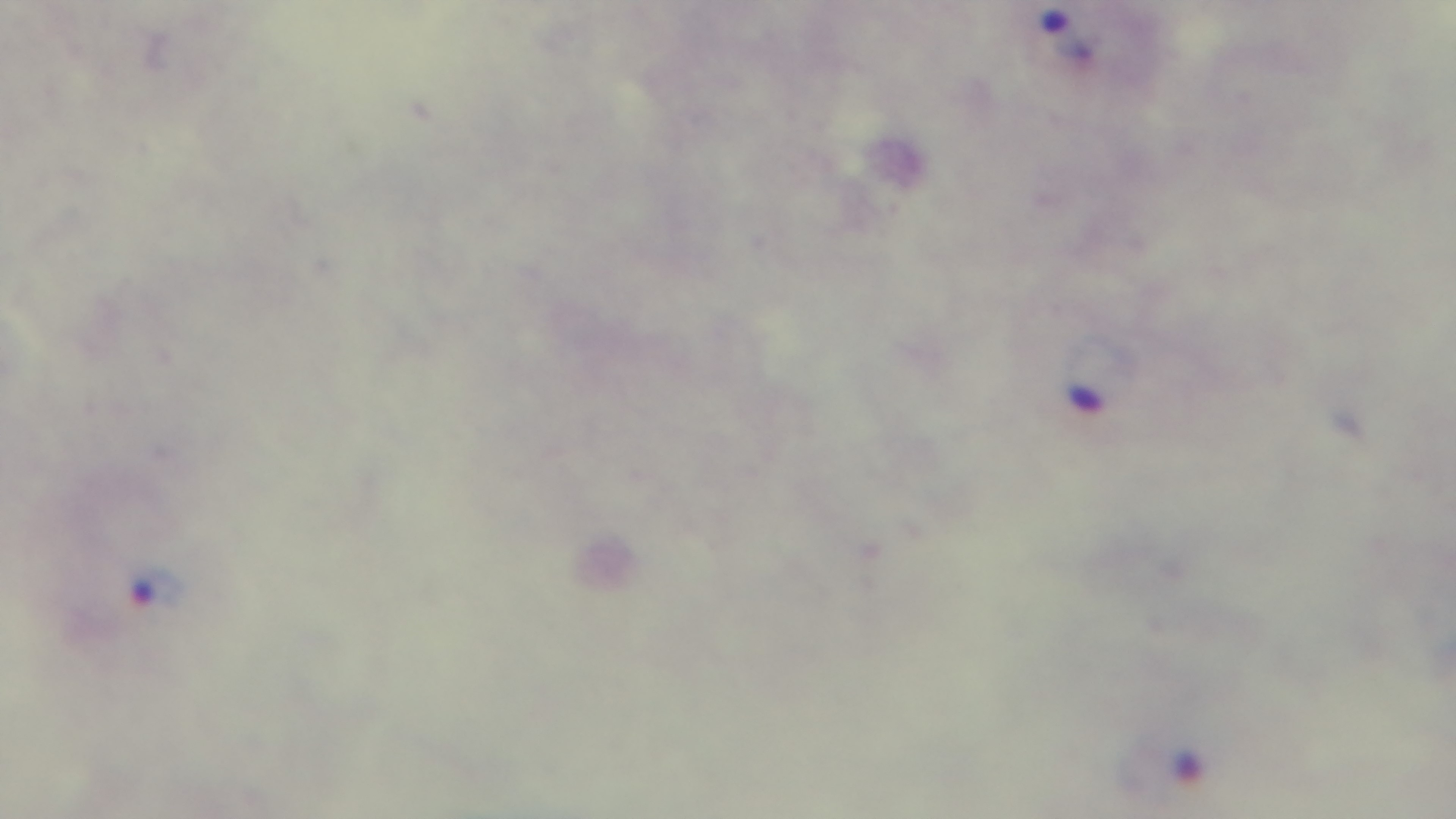
field of view = one from the slide
objective = 100x oil immersion
preparation = thick blood film
malaria status = infected
capture = mounted 4K digital camera
stain = Giemsa
modality = light microscopy